State which parasite is depicted.
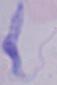
This is a trypanosome.

Captured at 1000x magnification. Photomicrograph.